Report the malaria status of this cell.
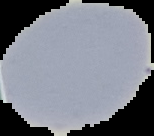

Uninfected.

Summary:
  - Image size: 154×136 pixels
  - Preparation: thin blood smear
  - Image type: segmented cell region with the area outside set to black